Classify this cell by malaria status.
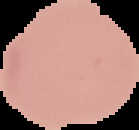
It is uninfected.

image type = segmented cell region with the area outside set to black
image size = 139×130 pixels
preparation = thin blood film